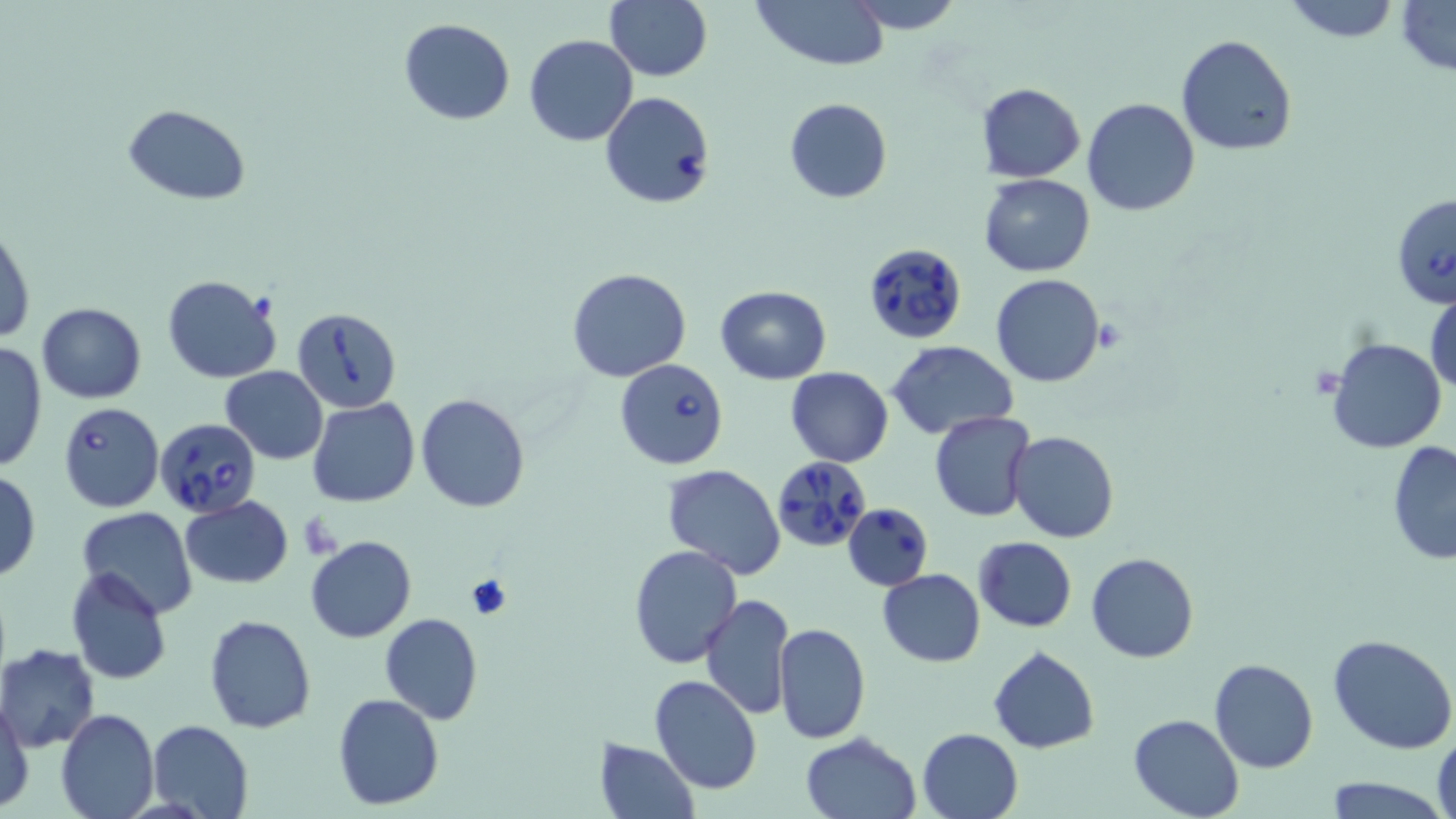
Approximate bounding boxes as named x1/y1/x2/y2 corners in pixels. Platelet locations: (x1=465, y1=573, x2=511, y2=620). Uninfected red blood cell locations: (x1=606, y1=0, x2=712, y2=83), (x1=752, y1=0, x2=889, y2=69), (x1=844, y1=0, x2=965, y2=33), (x1=1280, y1=0, x2=1402, y2=43), (x1=1396, y1=1, x2=1456, y2=75), (x1=398, y1=18, x2=516, y2=125), (x1=524, y1=34, x2=637, y2=146), (x1=1175, y1=34, x2=1297, y2=157), (x1=977, y1=84, x2=1085, y2=182), (x1=785, y1=98, x2=892, y2=203), (x1=1081, y1=98, x2=1201, y2=217), (x1=123, y1=103, x2=251, y2=204), (x1=978, y1=174, x2=1096, y2=277), (x1=1, y1=225, x2=35, y2=346), (x1=567, y1=267, x2=692, y2=382), (x1=990, y1=273, x2=1106, y2=387), (x1=162, y1=275, x2=282, y2=383), (x1=1426, y1=281, x2=1456, y2=400), (x1=715, y1=285, x2=831, y2=383), (x1=36, y1=302, x2=146, y2=403), (x1=1326, y1=336, x2=1446, y2=455), (x1=1, y1=339, x2=49, y2=473), (x1=887, y1=341, x2=1019, y2=437), (x1=220, y1=366, x2=329, y2=463), (x1=785, y1=366, x2=894, y2=466), (x1=416, y1=392, x2=530, y2=512), (x1=307, y1=398, x2=419, y2=507), (x1=930, y1=410, x2=1035, y2=522), (x1=1008, y1=431, x2=1119, y2=544), (x1=1386, y1=442, x2=1456, y2=565), (x1=661, y1=465, x2=786, y2=581), (x1=0, y1=467, x2=40, y2=582), (x1=179, y1=496, x2=295, y2=588), (x1=76, y1=506, x2=197, y2=616), (x1=305, y1=536, x2=417, y2=642), (x1=973, y1=536, x2=1077, y2=632), (x1=629, y1=544, x2=743, y2=667), (x1=1086, y1=553, x2=1199, y2=663), (x1=66, y1=565, x2=172, y2=684), (x1=877, y1=568, x2=986, y2=667), (x1=701, y1=594, x2=795, y2=721), (x1=204, y1=612, x2=316, y2=733), (x1=380, y1=614, x2=483, y2=726), (x1=774, y1=622, x2=871, y2=744), (x1=1328, y1=634, x2=1456, y2=755), (x1=1, y1=644, x2=101, y2=751), (x1=988, y1=646, x2=1100, y2=754), (x1=1208, y1=657, x2=1319, y2=773), (x1=649, y1=675, x2=762, y2=795), (x1=333, y1=693, x2=444, y2=809), (x1=0, y1=696, x2=34, y2=812), (x1=54, y1=708, x2=159, y2=818), (x1=1128, y1=713, x2=1245, y2=819), (x1=147, y1=719, x2=255, y2=819), (x1=917, y1=728, x2=1023, y2=818), (x1=1433, y1=730, x2=1456, y2=819), (x1=800, y1=732, x2=920, y2=818), (x1=594, y1=738, x2=700, y2=819), (x1=1322, y1=778, x2=1450, y2=817). Babesia divergens-infected red blood cell locations: (x1=601, y1=92, x2=716, y2=210), (x1=1392, y1=192, x2=1456, y2=310), (x1=862, y1=242, x2=968, y2=345), (x1=293, y1=305, x2=400, y2=412), (x1=615, y1=358, x2=728, y2=470), (x1=59, y1=402, x2=165, y2=513), (x1=158, y1=419, x2=261, y2=522), (x1=772, y1=455, x2=871, y2=552), (x1=843, y1=503, x2=933, y2=591). Slide-level diagnosis: Babesia divergens. May-Grünwald-Giemsa stain. Captured at 1000x magnification. Thin blood film. Single field of view. Optical microscopy. Image is 1456×819 pixels.